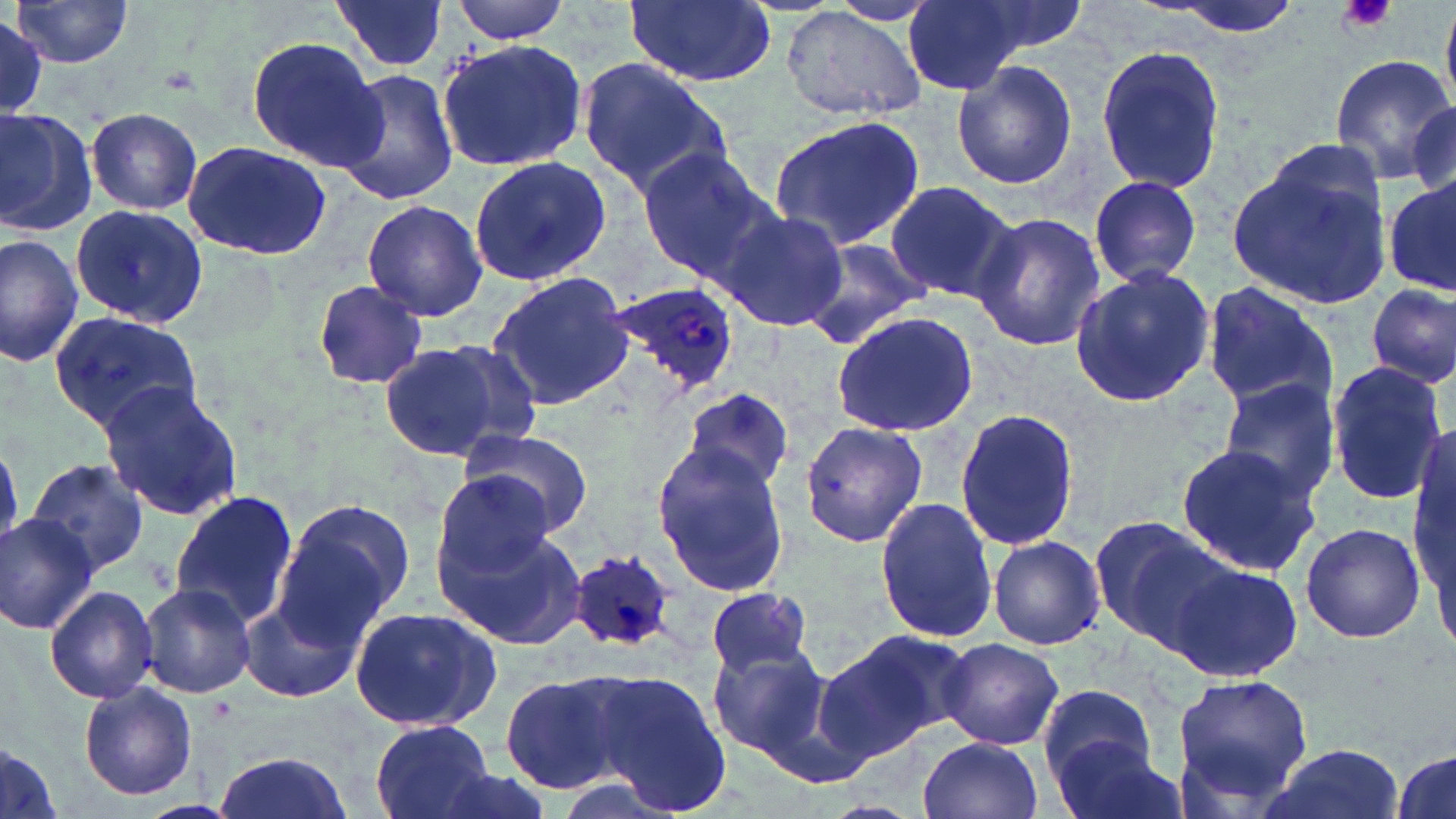

Summary:
  - Coordinate format: approximate bounding boxes as (x1,y1)-(x2,y2) corner pairs in pixels
  - Platelet locations: (1337,0)-(1397,34)
  - Plasmodium ovale-infected red blood cell locations: (602,279)-(740,396), (564,550)-(676,651)
  - Uninfected red blood cell locations: (331,0)-(448,74), (449,0)-(575,43), (623,0)-(776,87), (831,0)-(940,24), (901,0)-(1027,96), (946,0)-(1093,63), (1155,0)-(1310,43), (10,1)-(134,68), (781,7)-(927,124), (0,15)-(50,119), (246,37)-(385,171), (436,38)-(589,173), (1096,44)-(1226,196), (1328,54)-(1451,186), (578,60)-(734,197), (951,61)-(1078,189), (332,65)-(459,207), (1411,101)-(1456,204), (0,105)-(97,237), (86,107)-(203,215), (767,116)-(927,250), (183,141)-(333,262), (1232,147)-(1396,310), (635,149)-(774,282), (466,155)-(611,286), (1089,175)-(1203,284), (1382,177)-(1456,299), (884,180)-(1022,304), (360,199)-(488,321), (70,204)-(207,327), (708,206)-(849,334), (971,211)-(1103,354), (0,232)-(82,366), (801,235)-(936,349), (1068,266)-(1216,408), (488,270)-(636,407), (311,281)-(430,389), (1200,281)-(1339,413), (1366,282)-(1455,389), (49,311)-(203,431), (829,312)-(979,436), (378,341)-(521,461), (1326,358)-(1449,505), (1218,377)-(1343,502), (97,380)-(242,522), (679,387)-(794,493), (954,408)-(1080,551), (800,422)-(927,547), (458,428)-(592,538), (0,443)-(25,546), (1173,443)-(1321,575), (651,444)-(794,597), (28,459)-(150,578), (431,471)-(562,590), (170,492)-(299,628), (271,495)-(414,643), (875,498)-(996,642), (0,513)-(97,633), (1086,515)-(1229,649), (1300,521)-(1426,644), (438,523)-(588,653), (989,536)-(1104,649), (1164,561)-(1301,681), (137,581)-(255,698), (44,584)-(157,704), (706,587)-(818,679), (243,599)-(361,704), (349,606)-(503,734), (820,629)-(970,755), (940,637)-(1064,750), (708,649)-(832,762), (573,669)-(734,814), (500,671)-(628,792), (1171,672)-(1315,810), (80,682)-(197,802), (1038,682)-(1156,786), (371,719)-(494,819), (1050,734)-(1189,819), (919,735)-(1045,819), (0,739)-(64,819), (1254,742)-(1407,819), (1389,747)-(1455,819), (210,751)-(355,819)
  - Slide-level diagnosis: Plasmodium ovale
  - Magnification: 1000x
  - Field of view: one of a larger specimen
  - Stain: May-Grünwald-Giemsa
  - Preparation: thin blood film
  - Image size: 1456×819 pixels
  - Modality: optical microscopy